Assess this cell for malaria.
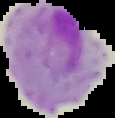
It is parasitized.

Summary:
  - Image type: segmented cell region on a black background
  - Preparation: thin blood film
  - Image size: 115×118 pixels